Locate every blood parasite and identify its species.
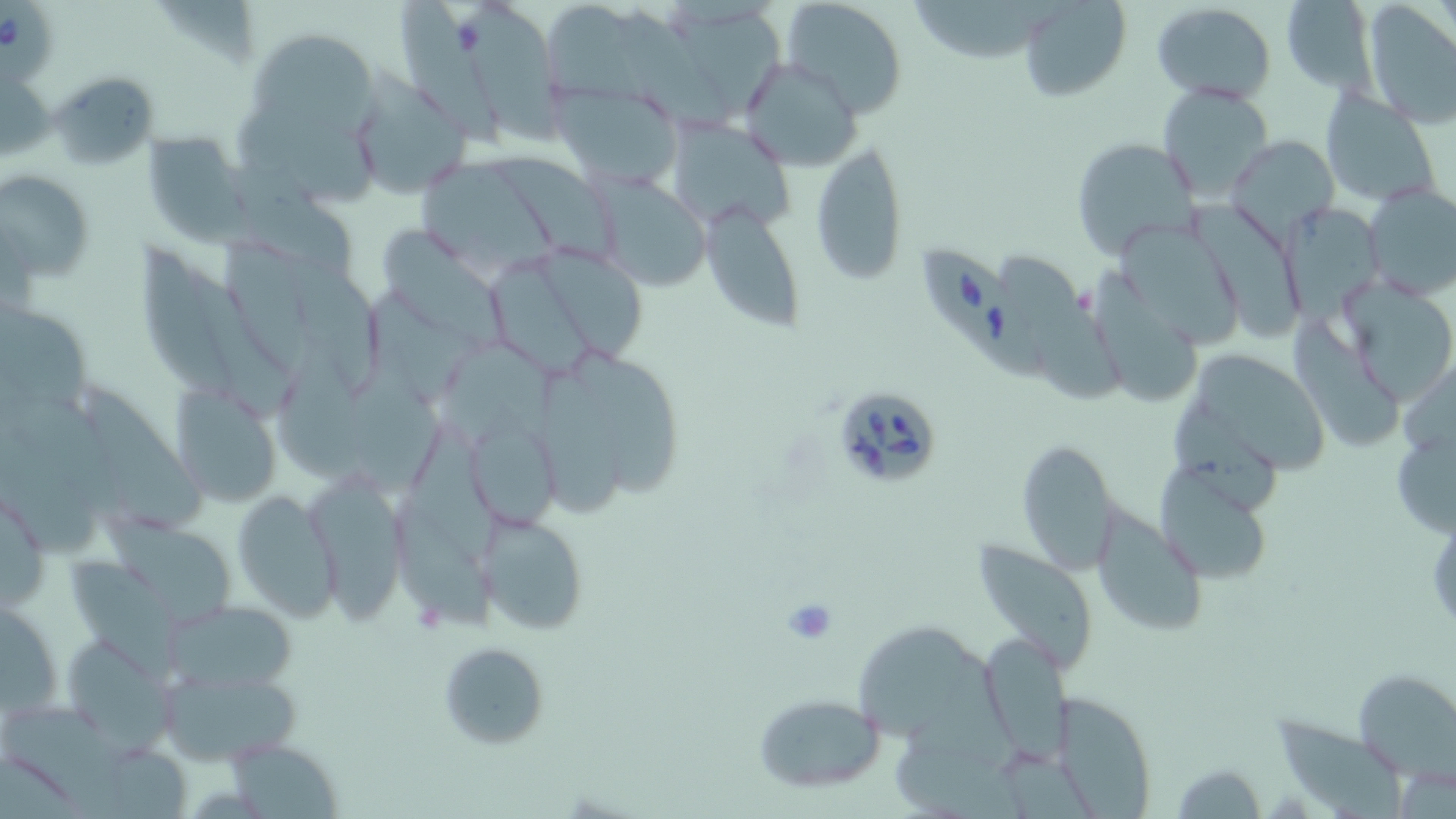
Approximate bounding boxes as named x1/y1/x2/y2 corners in pixels.
Babesia divergens-infected red blood cells: (x1=1, y1=1, x2=57, y2=70), (x1=919, y1=238, x2=1051, y2=387), (x1=827, y1=384, x2=946, y2=492).
No Plasmodium falciparum, Plasmodium ovale, Plasmodium malariae, Plasmodium vivax, or Trypanosoma brucei observed.

Summary:
  - Uninfected red blood cell locations: (x1=399, y1=0, x2=505, y2=151), (x1=463, y1=0, x2=571, y2=141), (x1=782, y1=0, x2=910, y2=117), (x1=913, y1=0, x2=1061, y2=59), (x1=1018, y1=0, x2=1132, y2=101), (x1=1279, y1=0, x2=1376, y2=91), (x1=1152, y1=2, x2=1276, y2=105), (x1=1360, y1=3, x2=1456, y2=126), (x1=161, y1=5, x2=266, y2=65), (x1=546, y1=5, x2=645, y2=103), (x1=671, y1=9, x2=778, y2=116), (x1=619, y1=13, x2=734, y2=133), (x1=255, y1=36, x2=379, y2=127), (x1=738, y1=55, x2=865, y2=172), (x1=48, y1=69, x2=160, y2=172), (x1=1, y1=72, x2=54, y2=162), (x1=350, y1=73, x2=471, y2=195), (x1=553, y1=82, x2=683, y2=193), (x1=1159, y1=84, x2=1273, y2=199), (x1=1321, y1=87, x2=1444, y2=206), (x1=241, y1=103, x2=379, y2=206), (x1=678, y1=120, x2=794, y2=230), (x1=142, y1=130, x2=250, y2=245), (x1=1225, y1=135, x2=1340, y2=242), (x1=1069, y1=138, x2=1198, y2=259), (x1=810, y1=139, x2=910, y2=286), (x1=498, y1=153, x2=622, y2=262), (x1=224, y1=160, x2=359, y2=281), (x1=420, y1=163, x2=554, y2=269), (x1=1, y1=170, x2=94, y2=284), (x1=591, y1=172, x2=708, y2=293), (x1=1361, y1=183, x2=1455, y2=302), (x1=1189, y1=195, x2=1303, y2=343), (x1=702, y1=203, x2=804, y2=335), (x1=1285, y1=204, x2=1381, y2=323), (x1=379, y1=217, x2=511, y2=347), (x1=1117, y1=227, x2=1242, y2=345), (x1=228, y1=238, x2=316, y2=367), (x1=533, y1=238, x2=647, y2=363), (x1=139, y1=244, x2=238, y2=396), (x1=999, y1=254, x2=1133, y2=407), (x1=286, y1=255, x2=386, y2=389), (x1=489, y1=263, x2=592, y2=377), (x1=1091, y1=264, x2=1206, y2=410), (x1=189, y1=270, x2=293, y2=423), (x1=1340, y1=281, x2=1456, y2=407), (x1=369, y1=288, x2=488, y2=406), (x1=0, y1=301, x2=89, y2=413), (x1=1282, y1=310, x2=1403, y2=452), (x1=343, y1=342, x2=443, y2=490), (x1=442, y1=342, x2=554, y2=451), (x1=281, y1=343, x2=360, y2=482), (x1=587, y1=346, x2=689, y2=503), (x1=1195, y1=352, x2=1333, y2=484), (x1=534, y1=363, x2=622, y2=521), (x1=168, y1=381, x2=287, y2=510), (x1=87, y1=382, x2=208, y2=536), (x1=1168, y1=397, x2=1286, y2=516), (x1=1, y1=415, x2=94, y2=560), (x1=459, y1=418, x2=563, y2=534), (x1=410, y1=422, x2=508, y2=562), (x1=1015, y1=436, x2=1120, y2=572), (x1=1397, y1=436, x2=1456, y2=536), (x1=1151, y1=453, x2=1269, y2=583), (x1=303, y1=470, x2=407, y2=623), (x1=0, y1=488, x2=50, y2=612), (x1=231, y1=490, x2=339, y2=622), (x1=393, y1=503, x2=498, y2=633), (x1=1092, y1=506, x2=1209, y2=637), (x1=101, y1=510, x2=236, y2=628), (x1=480, y1=512, x2=589, y2=637), (x1=974, y1=533, x2=1102, y2=674), (x1=67, y1=554, x2=183, y2=667), (x1=1, y1=597, x2=65, y2=718), (x1=163, y1=599, x2=300, y2=695), (x1=857, y1=615, x2=970, y2=743), (x1=978, y1=631, x2=1071, y2=761), (x1=61, y1=635, x2=175, y2=750), (x1=437, y1=641, x2=553, y2=751), (x1=157, y1=665, x2=302, y2=767), (x1=1354, y1=668, x2=1455, y2=777), (x1=752, y1=692, x2=887, y2=793), (x1=1050, y1=692, x2=1157, y2=816), (x1=4, y1=704, x2=129, y2=819), (x1=1276, y1=708, x2=1410, y2=815), (x1=222, y1=739, x2=345, y2=819), (x1=90, y1=742, x2=194, y2=817), (x1=893, y1=743, x2=1021, y2=818), (x1=1170, y1=761, x2=1268, y2=817)
  - Slide-level diagnosis: Babesia divergens
  - Field of view: single
  - Magnification: 1000x
  - Preparation: thin blood smear
  - Modality: optical microscopy
  - Image size: 1456×819 pixels
  - Stain: May-Grünwald-Giemsa